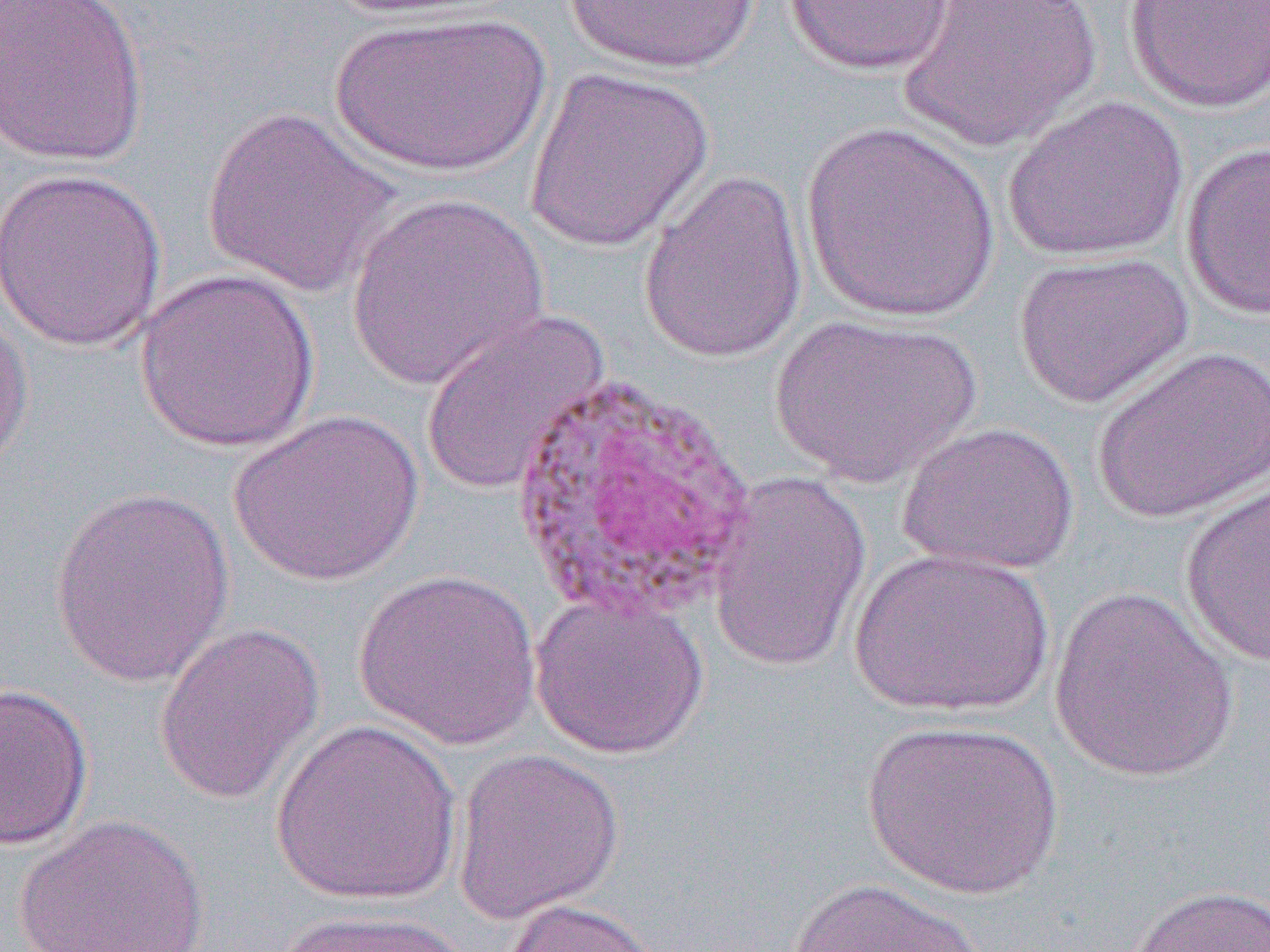

slide-level diagnosis = Plasmodium vivax
image size = 1270×952 pixels
modality = light microscopy
field of view = single
preparation = thin blood smear
uninfected red blood cell locations = approximate bounding boxes as (x1,y1)-(x2,y2) corner pairs in pixels: (1,0)-(150,168), (324,0)-(508,21), (563,0)-(763,74), (898,0)-(1102,150), (1124,0)-(1270,114), (780,1)-(960,77), (326,10)-(552,179), (524,66)-(716,253), (1004,94)-(1189,263), (201,106)-(402,298), (800,122)-(1001,323), (1180,140)-(1270,321), (0,166)-(168,352), (638,168)-(809,364), (345,193)-(551,391), (1013,250)-(1194,408), (135,268)-(320,453), (0,301)-(35,473), (419,309)-(611,497), (767,312)-(984,487), (1092,344)-(1270,524), (228,408)-(425,587), (898,420)-(1079,576), (704,470)-(873,674), (1179,479)-(1270,668), (47,485)-(235,689), (848,547)-(1055,719), (353,568)-(542,749), (1048,584)-(1241,782), (529,590)-(709,760), (152,620)-(325,806), (0,682)-(93,850), (269,718)-(464,906), (861,718)-(1065,899), (451,747)-(624,925), (12,813)-(211,952), (787,876)-(988,952), (1123,884)-(1270,952), (499,898)-(666,952), (272,909)-(477,951)
magnification = 1000x